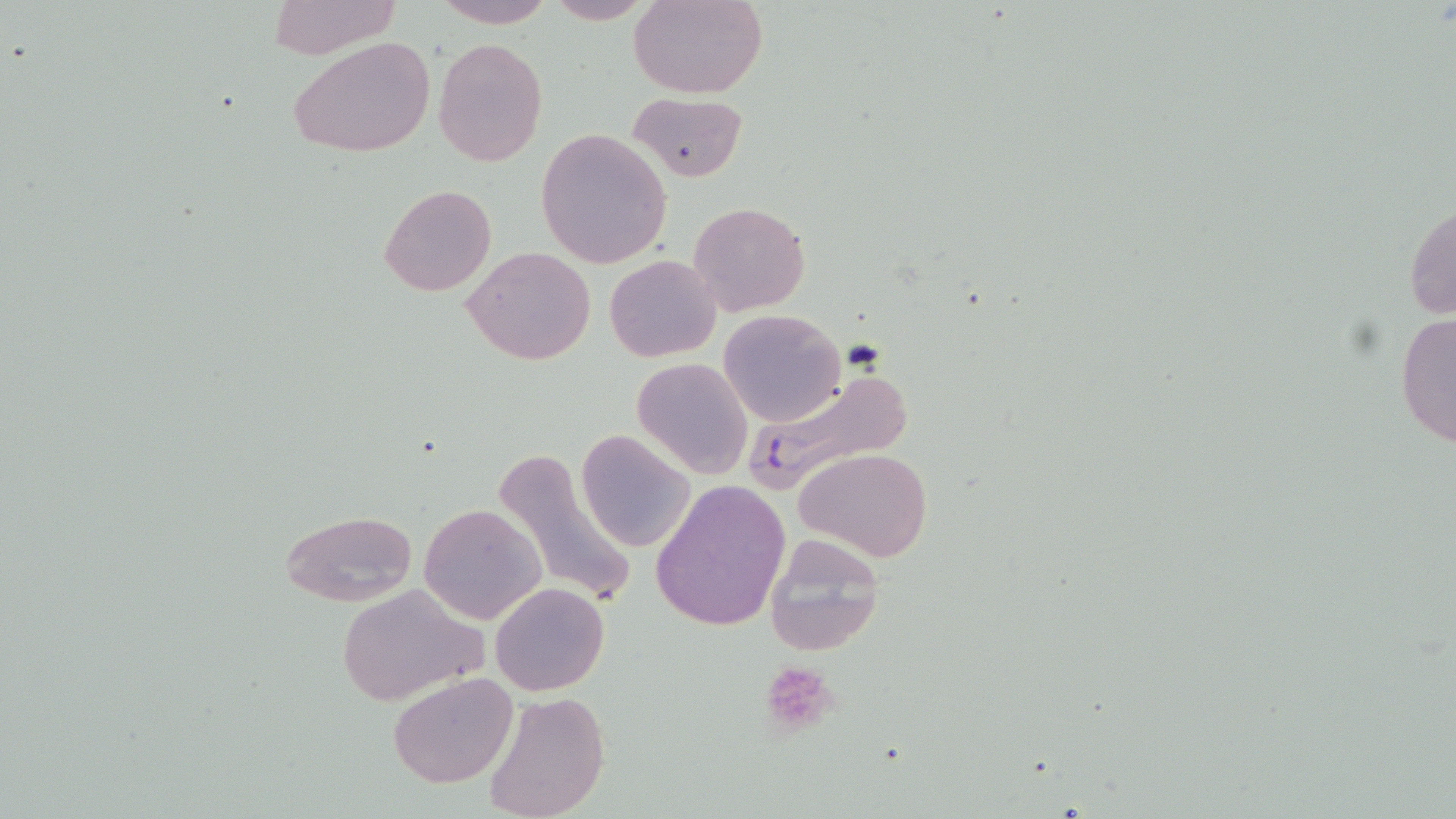
Summary:
  - Coordinate format: approximate bounding boxes as [x1, y1, x2, y2] in pixels
  - Platelet locations: [757, 660, 838, 740]
  - Uninfected red blood cell locations: [267, 0, 403, 58], [431, 0, 557, 28], [541, 0, 657, 24], [629, 0, 769, 99], [288, 35, 436, 158], [434, 38, 547, 167], [629, 92, 747, 182], [538, 128, 671, 268], [378, 185, 495, 297], [1405, 194, 1455, 326], [687, 202, 810, 316], [463, 245, 596, 365], [604, 254, 721, 363], [1394, 308, 1455, 452], [719, 309, 844, 426], [632, 357, 753, 478], [575, 430, 695, 552], [492, 447, 637, 608], [795, 447, 934, 563], [650, 481, 792, 631], [418, 502, 547, 624], [279, 509, 418, 606], [762, 534, 887, 658], [333, 583, 484, 708], [490, 583, 610, 697], [388, 673, 517, 788], [480, 691, 613, 819]
  - Plasmodium falciparum-infected red blood cell locations: [746, 366, 916, 489]
  - Slide-level diagnosis: Plasmodium falciparum
  - Image size: 1456×819 pixels
  - Magnification: 1000x
  - Preparation: thin blood smear
  - Stain: May-Grünwald-Giemsa
  - Modality: optical microscopy
  - Field of view: one of a larger specimen